Assess this cell for malaria.
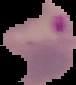
Parasitized.

Cell region segmented out of the field of view; the surrounding area is masked to black. Image is 76×85 pixels. From a thin blood film.